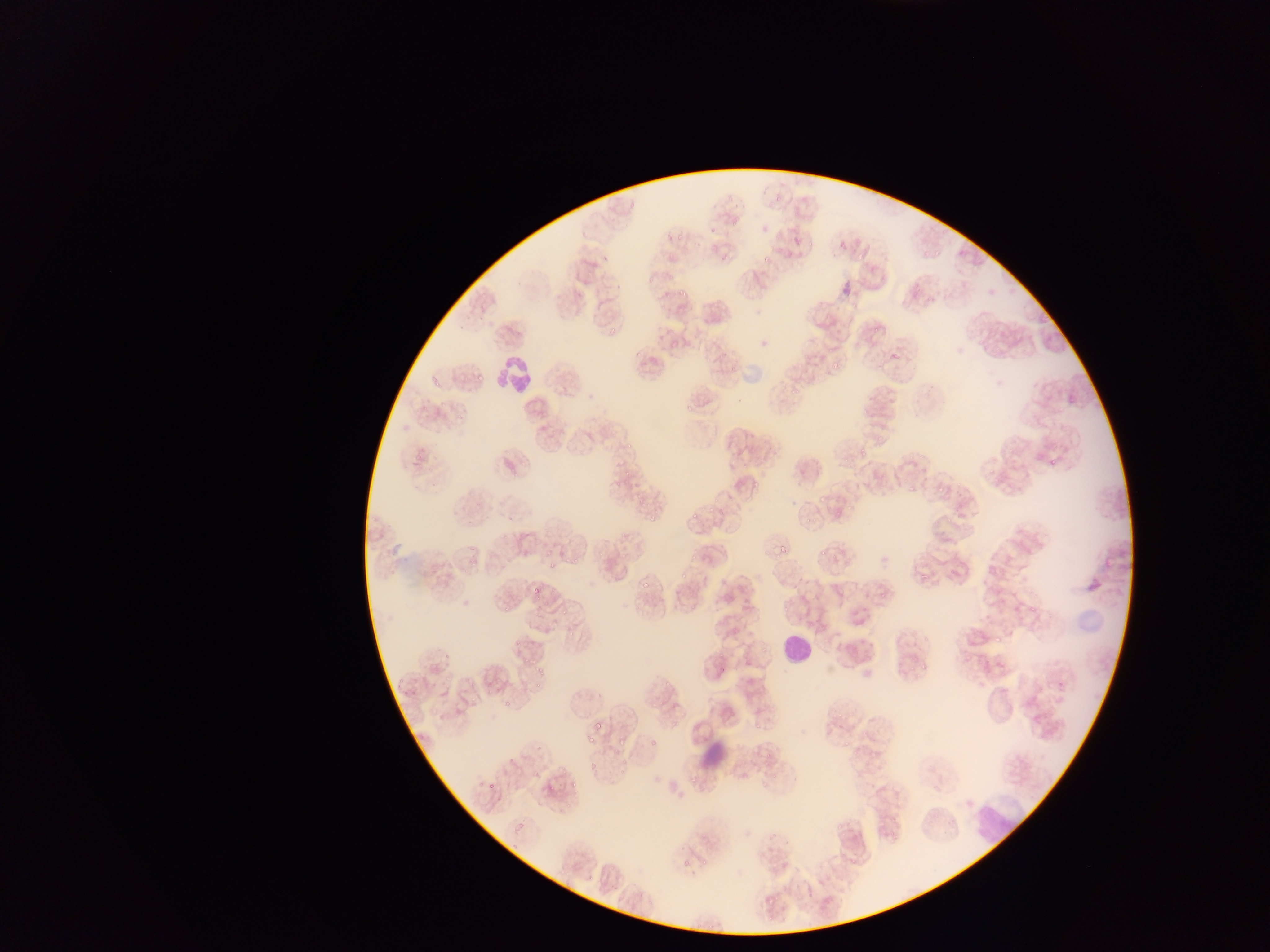

Approximate bounding boxes as [left, top, right, bottom] in pixels.
Summary:
  - Plasmodium parasite locations: [709, 226, 717, 236], [666, 235, 675, 243], [920, 247, 928, 259], [932, 248, 944, 266], [758, 251, 775, 264], [570, 279, 592, 300], [676, 287, 686, 298], [922, 295, 936, 306], [599, 326, 617, 339], [869, 326, 880, 334], [670, 343, 683, 357], [891, 347, 902, 359], [633, 348, 642, 357], [828, 354, 846, 371], [473, 362, 495, 385], [430, 371, 437, 393], [786, 384, 805, 398], [1063, 385, 1080, 408], [685, 397, 695, 413], [861, 397, 879, 415], [454, 411, 464, 421], [623, 442, 631, 458], [856, 446, 866, 459], [409, 448, 425, 467], [1049, 454, 1057, 466], [503, 460, 516, 473], [618, 470, 631, 479], [750, 477, 763, 494], [901, 480, 920, 494], [937, 483, 947, 495], [635, 491, 646, 505], [815, 492, 825, 503], [845, 497, 860, 511], [707, 508, 718, 517], [647, 509, 657, 520], [689, 509, 701, 519], [803, 512, 816, 524], [944, 516, 952, 524], [777, 537, 799, 558], [839, 541, 851, 558], [619, 545, 632, 562], [543, 546, 554, 555], [819, 546, 829, 560], [830, 548, 843, 559], [465, 550, 478, 562], [687, 553, 700, 560], [565, 558, 580, 565], [546, 561, 557, 578], [678, 572, 689, 581], [916, 574, 933, 588], [528, 582, 541, 600], [639, 582, 654, 594], [1030, 594, 1040, 616], [742, 598, 752, 611], [499, 603, 512, 615], [534, 604, 543, 617], [559, 607, 568, 618], [511, 625, 534, 655], [993, 638, 1003, 647], [441, 650, 452, 665], [916, 659, 931, 676], [533, 664, 550, 682], [395, 671, 408, 690], [660, 672, 674, 689], [485, 678, 495, 695], [531, 680, 540, 699], [502, 691, 525, 711], [471, 693, 477, 705], [828, 707, 845, 724], [756, 719, 765, 731], [717, 721, 734, 728], [594, 722, 604, 732], [585, 731, 594, 742], [618, 731, 632, 750], [867, 732, 884, 764], [835, 734, 853, 756], [648, 740, 659, 745], [615, 750, 633, 775], [758, 752, 774, 759], [587, 753, 602, 778], [531, 770, 540, 779], [564, 772, 585, 793], [687, 777, 702, 790], [755, 778, 769, 795], [484, 781, 496, 794], [543, 784, 553, 794], [508, 820, 529, 834], [743, 830, 751, 839], [765, 901, 786, 914]
  - Leukocyte locations: [501, 331, 539, 402], [783, 632, 810, 660], [972, 800, 1018, 844]
  - Country: Ghana
  - Image size: 1270×952 pixels
  - Capture: mobile-phone photograph through a microscope
  - Field of view: single
  - Preparation: thin blood film